Report the malaria status of this cell.
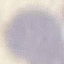
Uninfected.

Giemsa stain. Acquired by smartphone through the microscope eyepiece. Thin smear of blood. Automatically extracted cell patch, resized to 64 × 64 pixels.